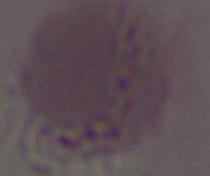
{
  "modality": "micrograph",
  "magnification": "1000x",
  "identification": "red blood cell"
}